Report the malaria status of this cell.
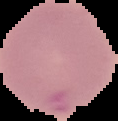
Uninfected.

image type = segmented cell region with the area outside set to black
image size = 118×121 pixels
preparation = thin blood film